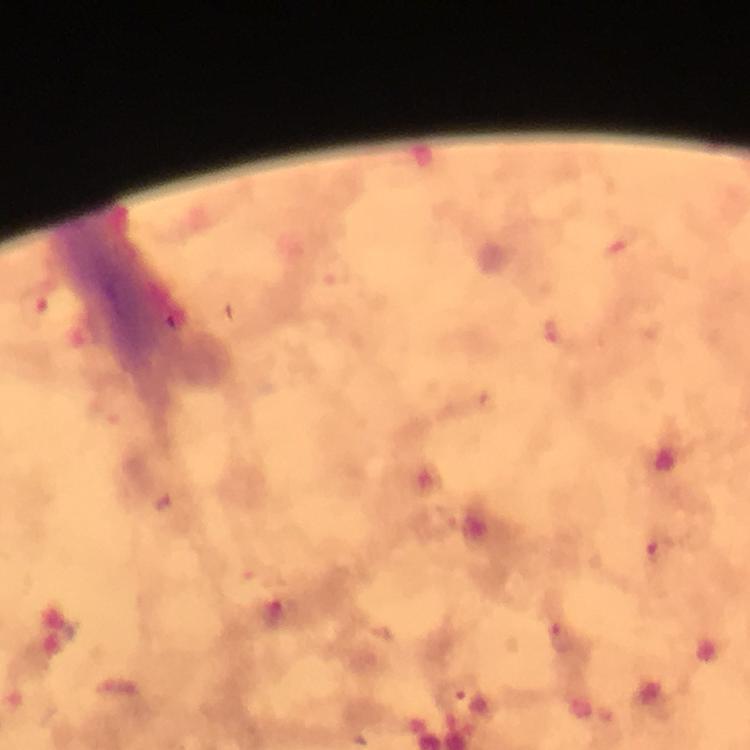
magnification = 100x
preparation = thick smear
image size = 750×750 pixels
cropped from = a single field of view
capture = smartphone camera through the microscope
immersion oil = used
stain = Giemsa
context = from a diagnostic examination for malaria
Plasmodium parasite locations = approximate centers as {x, y} in pixels: {550, 333}, {658, 551}, {273, 614}, {562, 636}, {460, 698}